Comment on the morphology of the erythrocytes.
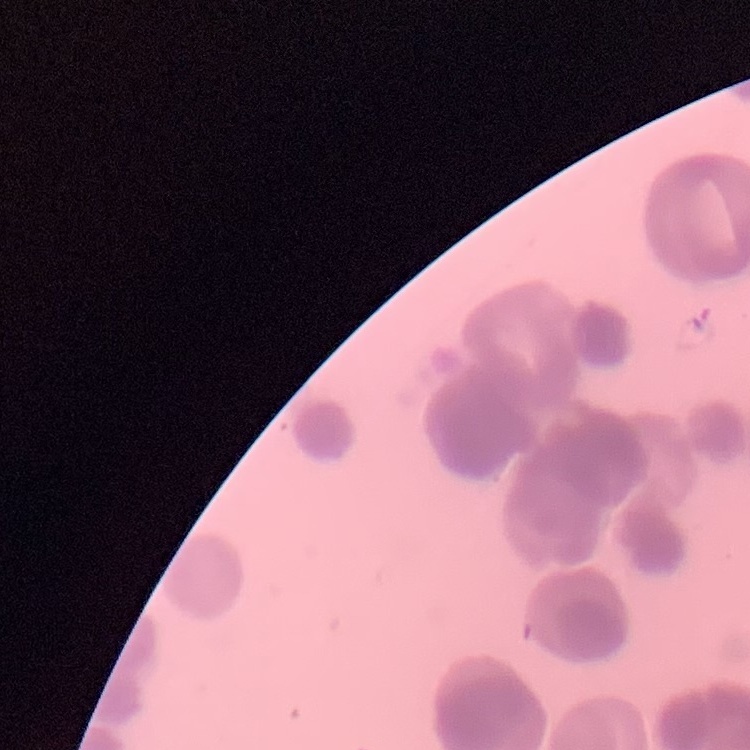

Rouleaux formation.

Summary:
  - Image type: one tile cut from a larger photomicrograph
  - Preparation: thin blood film
  - Stain: Field's or Giemsa